Assess this cell for malaria.
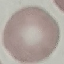
Uninfected.

Automatically extracted cell patch, resized to 64 × 64 pixels. Thin blood smear. Giemsa-stained preparation. Photographed with a smartphone camera at the microscope eyepiece.